Give the extent of all Plasmodium falciparum-infected red blood cells.
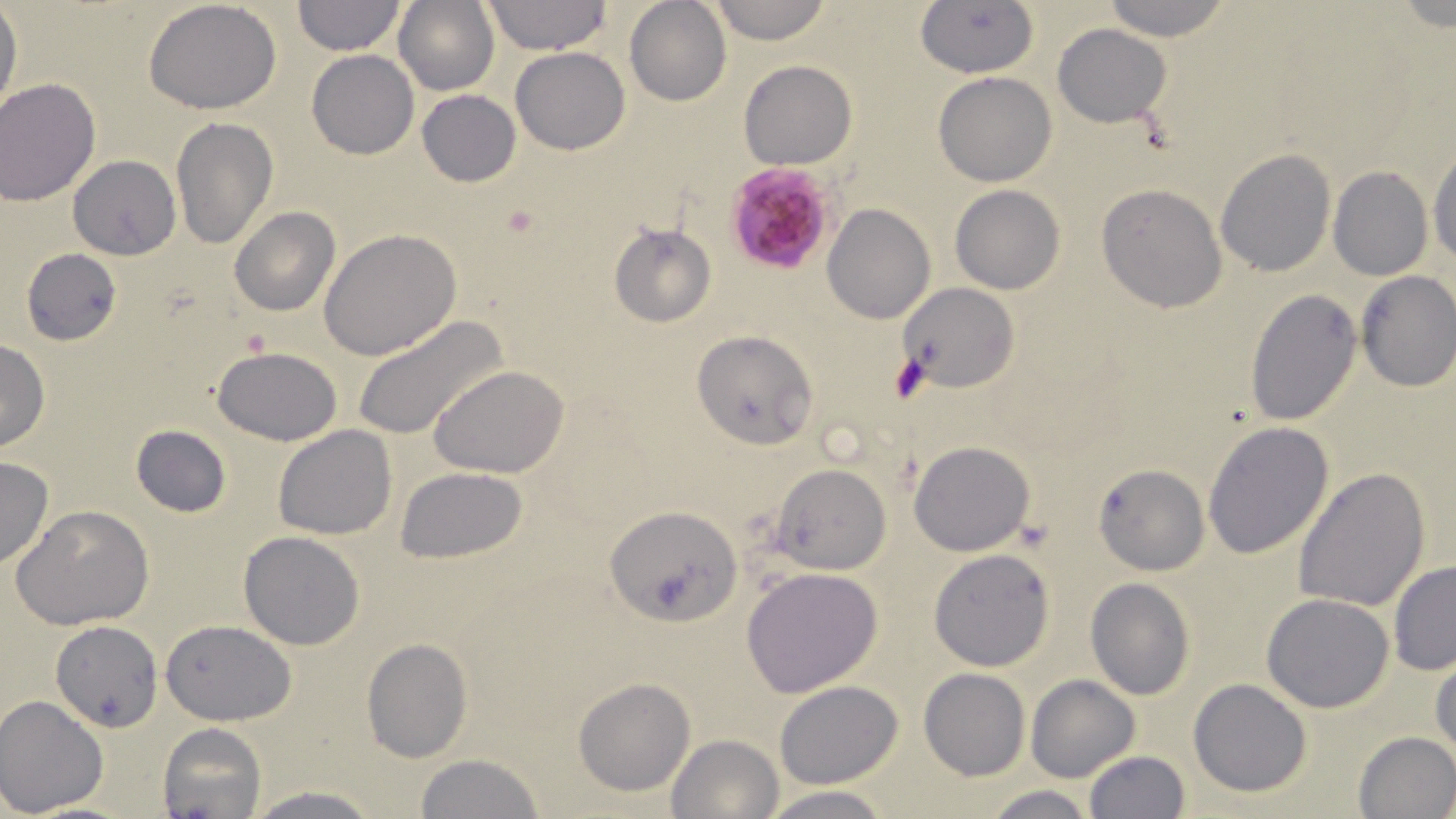
Approximate bounding boxes as (x1, y1, x2, y2) in pixels.
Plasmodium falciparum-infected red blood cells: (725, 163, 836, 275).

slide-level diagnosis = Plasmodium falciparum
modality = optical microscopy
preparation = thin blood smear
stain = May-Grünwald-Giemsa
image size = 1456×819 pixels
field of view = one of a larger specimen
magnification = 1000x
platelet locations = approximate bounding boxes as (x1, y1, x2, y2) in pixels: (501, 206, 541, 241), (242, 326, 273, 357), (887, 353, 931, 405)
uninfected red blood cell locations = approximate bounding boxes as (x1, y1, x2, y2) in pixels: (291, 0, 407, 55), (624, 0, 731, 106), (708, 0, 834, 45), (915, 0, 1039, 78), (1102, 0, 1233, 41), (392, 1, 500, 96), (480, 1, 611, 54), (143, 2, 284, 115), (0, 9, 22, 117), (1053, 23, 1173, 128), (511, 46, 630, 154), (306, 49, 419, 159), (738, 59, 857, 168), (932, 72, 1057, 187), (0, 78, 102, 206), (417, 90, 520, 187), (171, 118, 277, 250), (1429, 146, 1456, 268), (1215, 148, 1336, 277), (69, 156, 181, 260), (1327, 167, 1434, 281), (1096, 183, 1228, 314), (949, 185, 1064, 293), (823, 202, 936, 323), (229, 206, 340, 317), (608, 222, 718, 328), (319, 228, 462, 360), (21, 247, 121, 346), (1355, 272, 1456, 392), (895, 283, 1020, 394), (1245, 287, 1364, 425), (352, 314, 506, 443), (691, 328, 818, 451), (0, 341, 52, 451), (212, 346, 342, 446), (430, 365, 570, 478), (1202, 420, 1334, 560), (130, 424, 233, 517), (272, 424, 398, 541), (909, 440, 1034, 555), (0, 455, 53, 569), (771, 463, 893, 575), (1093, 464, 1209, 575), (1293, 466, 1431, 613), (396, 467, 527, 562), (12, 504, 154, 630), (605, 505, 741, 626), (238, 530, 367, 650), (929, 548, 1054, 670), (1388, 560, 1456, 675), (741, 567, 883, 697), (1085, 578, 1195, 699), (1262, 593, 1395, 713), (161, 618, 296, 724), (50, 619, 163, 731), (362, 639, 472, 762), (1431, 648, 1456, 760), (919, 668, 1031, 780), (1025, 674, 1140, 782), (574, 678, 694, 796), (1189, 678, 1313, 797), (774, 681, 903, 789), (0, 695, 109, 817), (157, 722, 268, 819), (1352, 730, 1456, 819), (667, 734, 781, 818), (1082, 751, 1191, 818), (413, 754, 550, 818), (980, 784, 1097, 819), (243, 785, 384, 818), (761, 785, 893, 819)